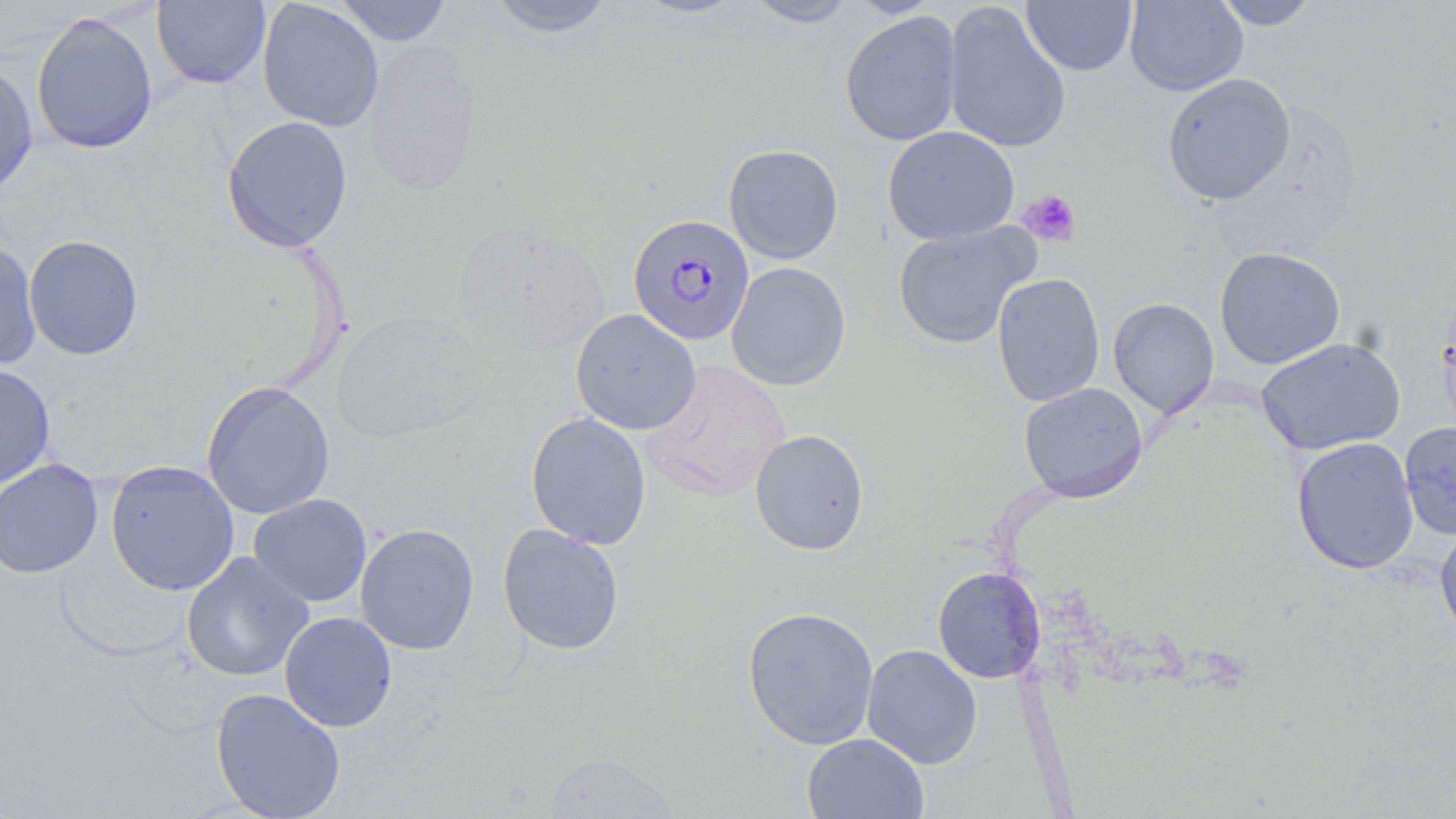

Approximate bounding boxes as [x1, y1, x2, y2] in pixels. Plasmodium falciparum-infected red blood cell locations: [628, 214, 755, 344]. Platelet locations: [1017, 189, 1081, 246]. Uninfected red blood cell locations: [258, 0, 383, 132], [333, 0, 453, 45], [485, 0, 617, 38], [629, 0, 747, 19], [744, 0, 859, 28], [845, 0, 943, 18], [1022, 0, 1137, 76], [1124, 0, 1247, 96], [1212, 0, 1319, 30], [152, 1, 271, 89], [943, 1, 1071, 155], [840, 10, 963, 147], [30, 12, 159, 155], [363, 40, 482, 199], [0, 59, 38, 197], [1161, 72, 1296, 206], [222, 115, 353, 253], [882, 125, 1020, 245], [723, 144, 844, 264], [451, 219, 609, 357], [893, 220, 1040, 350], [24, 235, 144, 360], [0, 240, 42, 371], [1214, 247, 1346, 369], [726, 262, 851, 390], [991, 272, 1105, 407], [1437, 284, 1456, 438], [1108, 296, 1219, 419], [570, 308, 701, 436], [333, 309, 488, 443], [1255, 337, 1405, 456], [641, 360, 791, 501], [0, 364, 56, 493], [201, 380, 335, 519], [1019, 382, 1148, 503], [525, 411, 652, 549], [1399, 421, 1456, 541], [750, 429, 870, 555], [1291, 436, 1419, 574], [0, 458, 104, 579], [105, 460, 240, 595], [248, 493, 372, 608], [354, 523, 480, 655], [497, 523, 625, 655], [1435, 523, 1456, 645], [181, 552, 315, 682], [932, 566, 1046, 683], [742, 605, 879, 750], [279, 611, 398, 732], [862, 644, 982, 769], [210, 688, 346, 819], [801, 733, 929, 819], [545, 753, 678, 818]. Slide-level diagnosis: Plasmodium falciparum. Single field of view. Captured at 1000x magnification. Optical microscopy. Thin blood smear. May-Grünwald-Giemsa-stained preparation. Image is 1456×819 pixels.